Describe the morphology of the erythrocytes.
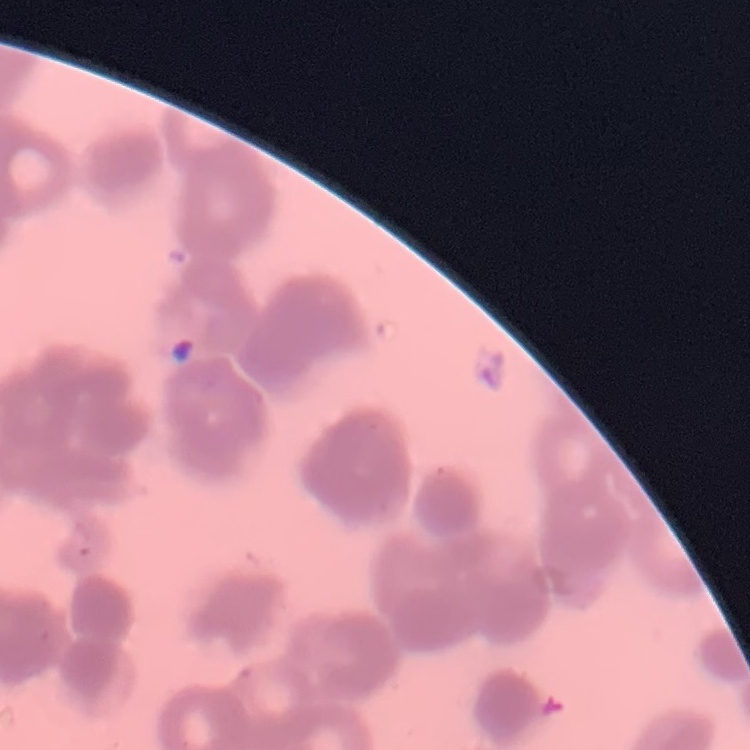
They show rouleaux formation.

Field's or Giemsa stain. One tile cut from a larger photomicrograph. Thin blood film.